Describe the morphology of the erythrocytes.
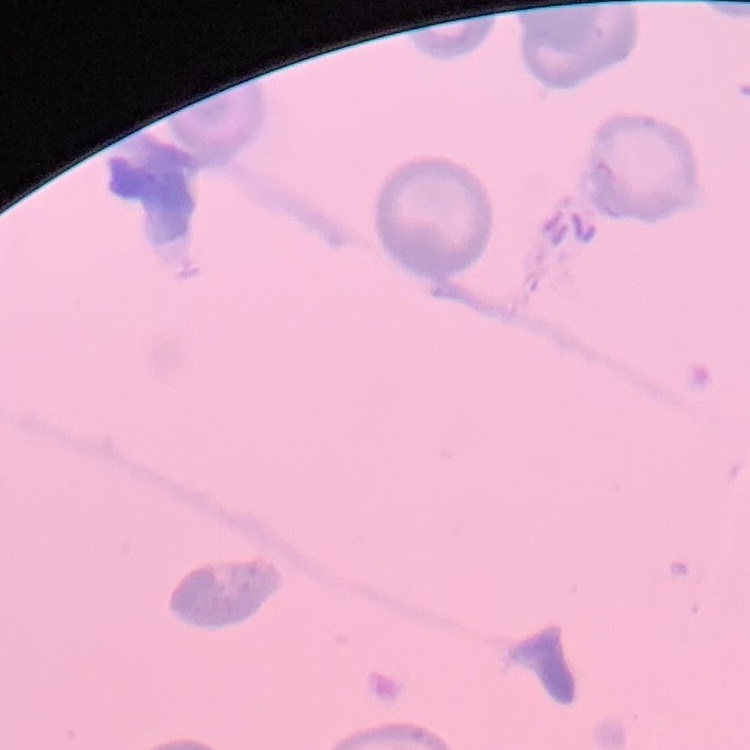

They show no rouleaux formation.

stain = Field's or Giemsa
image type = square crop of a larger photomicrograph
preparation = thin peripheral smear